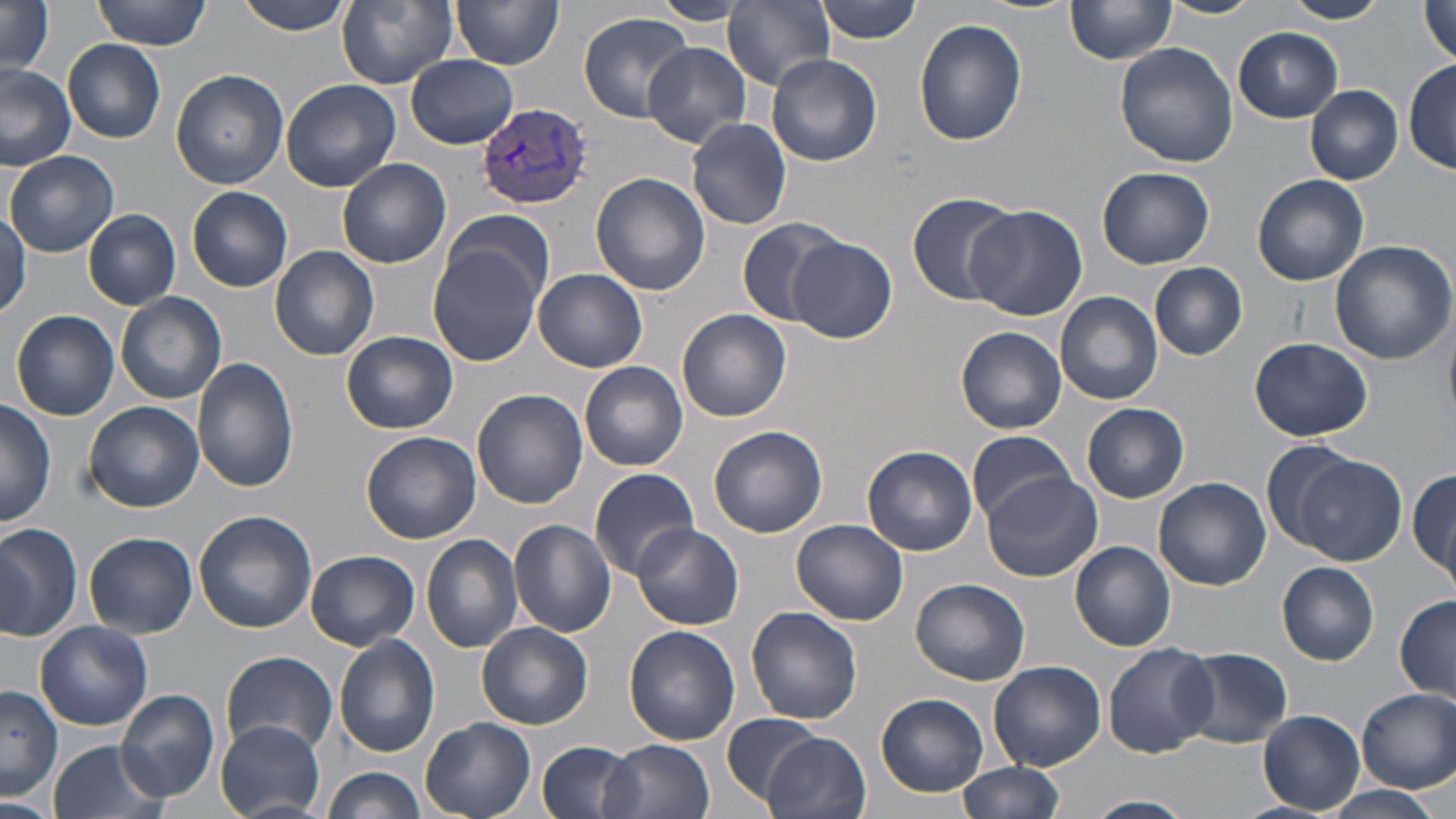

Summary:
  - Coordinate format: approximate bounding boxes as named x1/y1/x2/y2 corners in pixels
  - Uninfected red blood cell locations: (x1=94, y1=0, x2=214, y2=50), (x1=233, y1=0, x2=360, y2=36), (x1=335, y1=0, x2=458, y2=89), (x1=725, y1=0, x2=837, y2=89), (x1=815, y1=0, x2=923, y2=43), (x1=1065, y1=0, x2=1177, y2=64), (x1=1159, y1=0, x2=1263, y2=19), (x1=1282, y1=0, x2=1388, y2=24), (x1=452, y1=1, x2=563, y2=71), (x1=1418, y1=2, x2=1456, y2=65), (x1=0, y1=3, x2=56, y2=76), (x1=579, y1=12, x2=695, y2=122), (x1=915, y1=19, x2=1027, y2=146), (x1=1233, y1=26, x2=1343, y2=122), (x1=64, y1=40, x2=166, y2=142), (x1=643, y1=42, x2=750, y2=146), (x1=1116, y1=42, x2=1240, y2=168), (x1=406, y1=55, x2=517, y2=147), (x1=767, y1=55, x2=882, y2=166), (x1=1405, y1=59, x2=1456, y2=174), (x1=0, y1=64, x2=76, y2=168), (x1=171, y1=68, x2=289, y2=188), (x1=280, y1=79, x2=401, y2=191), (x1=1305, y1=84, x2=1404, y2=184), (x1=686, y1=119, x2=792, y2=231), (x1=6, y1=150, x2=119, y2=257), (x1=337, y1=158, x2=451, y2=269), (x1=1098, y1=167, x2=1214, y2=268), (x1=590, y1=172, x2=710, y2=296), (x1=1252, y1=175, x2=1369, y2=286), (x1=188, y1=186, x2=293, y2=292), (x1=907, y1=192, x2=1022, y2=305), (x1=966, y1=207, x2=1088, y2=322), (x1=443, y1=208, x2=556, y2=315), (x1=0, y1=209, x2=29, y2=318), (x1=84, y1=210, x2=181, y2=310), (x1=735, y1=216, x2=850, y2=328), (x1=787, y1=236, x2=897, y2=344), (x1=427, y1=240, x2=545, y2=368), (x1=1329, y1=240, x2=1456, y2=366), (x1=270, y1=245, x2=379, y2=361), (x1=1151, y1=263, x2=1247, y2=360), (x1=535, y1=269, x2=648, y2=372), (x1=116, y1=291, x2=226, y2=403), (x1=1055, y1=291, x2=1164, y2=405), (x1=9, y1=303, x2=230, y2=412), (x1=676, y1=309, x2=791, y2=422), (x1=11, y1=310, x2=119, y2=421), (x1=1444, y1=320, x2=1456, y2=425), (x1=957, y1=327, x2=1067, y2=434), (x1=342, y1=331, x2=458, y2=434), (x1=1248, y1=336, x2=1374, y2=442), (x1=193, y1=357, x2=299, y2=492), (x1=580, y1=360, x2=689, y2=471), (x1=473, y1=389, x2=588, y2=508), (x1=0, y1=399, x2=56, y2=527), (x1=83, y1=401, x2=203, y2=513), (x1=1081, y1=403, x2=1190, y2=503), (x1=708, y1=426, x2=827, y2=538), (x1=967, y1=429, x2=1074, y2=522), (x1=361, y1=431, x2=480, y2=544), (x1=1259, y1=438, x2=1367, y2=550), (x1=862, y1=445, x2=979, y2=555), (x1=1289, y1=453, x2=1406, y2=565), (x1=1409, y1=466, x2=1456, y2=586), (x1=589, y1=467, x2=702, y2=577), (x1=984, y1=472, x2=1103, y2=583), (x1=1155, y1=477, x2=1271, y2=590), (x1=538, y1=478, x2=673, y2=615), (x1=194, y1=509, x2=318, y2=632), (x1=509, y1=519, x2=616, y2=638), (x1=792, y1=519, x2=908, y2=624), (x1=631, y1=523, x2=744, y2=631), (x1=0, y1=526, x2=83, y2=639), (x1=84, y1=532, x2=197, y2=637), (x1=421, y1=534, x2=524, y2=655), (x1=1070, y1=541, x2=1175, y2=651), (x1=305, y1=550, x2=420, y2=650), (x1=1278, y1=563, x2=1379, y2=664), (x1=912, y1=577, x2=1030, y2=685), (x1=1395, y1=595, x2=1455, y2=705), (x1=746, y1=605, x2=863, y2=724), (x1=35, y1=620, x2=153, y2=730), (x1=478, y1=623, x2=592, y2=727), (x1=624, y1=627, x2=739, y2=746), (x1=335, y1=634, x2=441, y2=758), (x1=1104, y1=643, x2=1217, y2=758), (x1=1175, y1=646, x2=1295, y2=749), (x1=222, y1=651, x2=339, y2=759), (x1=989, y1=661, x2=1106, y2=770), (x1=0, y1=686, x2=61, y2=801), (x1=1355, y1=687, x2=1456, y2=793), (x1=117, y1=690, x2=219, y2=801), (x1=877, y1=693, x2=989, y2=797), (x1=1260, y1=710, x2=1365, y2=815), (x1=720, y1=712, x2=823, y2=809), (x1=420, y1=717, x2=536, y2=819), (x1=215, y1=721, x2=326, y2=819), (x1=762, y1=731, x2=871, y2=819), (x1=46, y1=739, x2=169, y2=819), (x1=537, y1=739, x2=640, y2=819), (x1=599, y1=739, x2=715, y2=819), (x1=957, y1=762, x2=1063, y2=819), (x1=322, y1=768, x2=427, y2=819), (x1=1311, y1=786, x2=1446, y2=819), (x1=1083, y1=795, x2=1196, y2=819), (x1=0, y1=799, x2=56, y2=819)
  - Plasmodium vivax-infected red blood cell locations: (x1=478, y1=104, x2=592, y2=211)
  - Slide-level diagnosis: Plasmodium vivax
  - Preparation: thin blood film
  - Magnification: 1000x
  - Modality: light microscopy
  - Field of view: one of a larger specimen
  - Image size: 1456×819 pixels
  - Stain: May-Grünwald-Giemsa